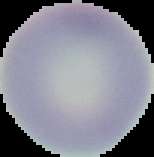

preparation = thin blood smear
image type = segmented cell region with the area outside set to black
malaria status = uninfected
image size = 154×157 pixels